Point out each Plasmodium parasite.
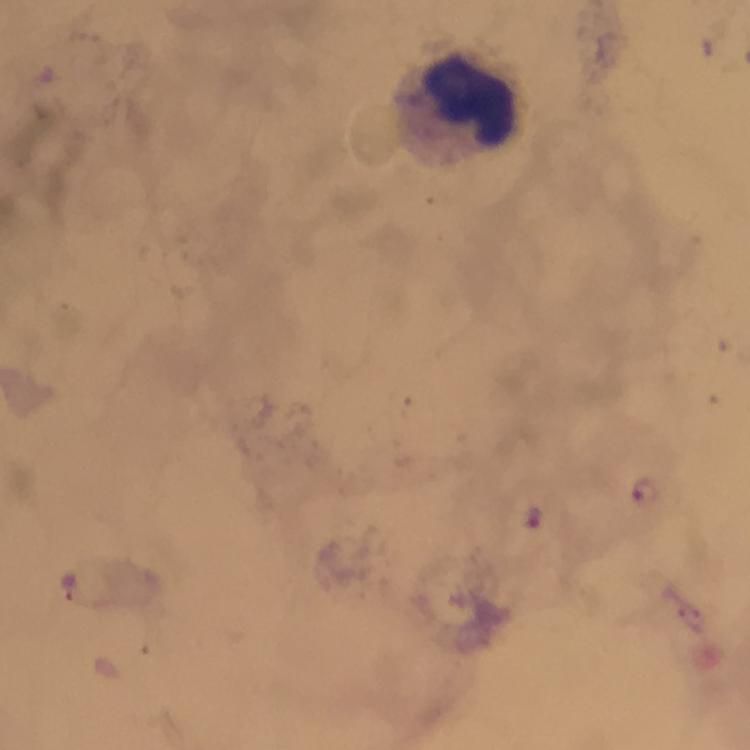
Approximate object centers, in pixels from the top-left corner.
Plasmodium parasites: (x=642, y=489), (x=533, y=516).

Leukocyte locations: (x=470, y=100). From a malaria diagnostic workup. 100x magnification. Giemsa-stained preparation. Thick blood film. Image is 750×750 pixels. Photographed through the microscope with a smartphone camera. Immersion oil was used. Cropped region of a single field of view.